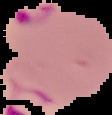
Summary:
  - Malaria status: parasitized
  - Image type: segmented cell region on a black background
  - Preparation: thin blood film
  - Image size: 112×115 pixels